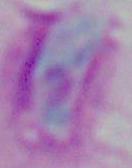

Summary:
  - Identification: Toxoplasma gondii
  - Magnification: 1000x
  - Modality: photomicrograph